Comment on the morphology of the erythrocytes.
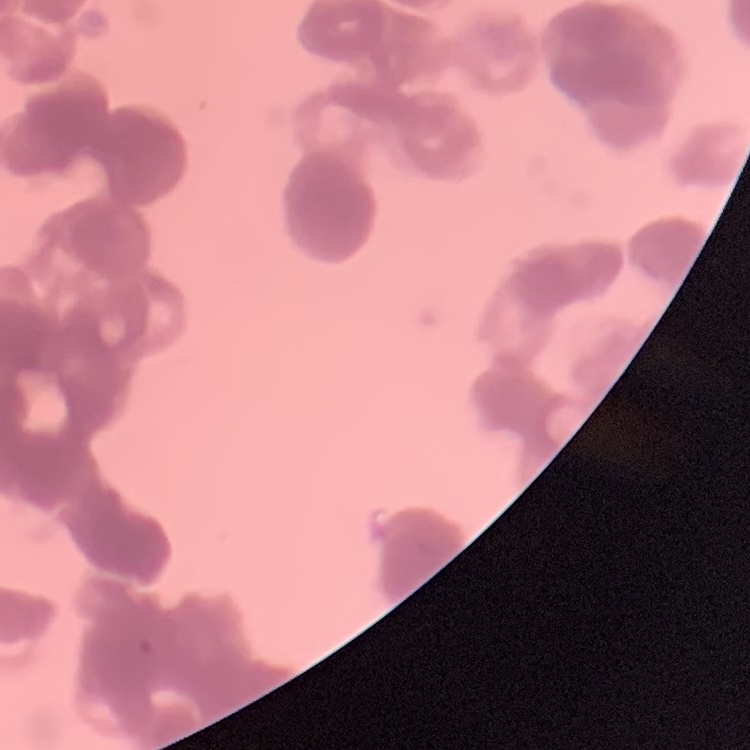

They show rouleaux formation.

One tile cut from a larger photomicrograph. Stained with either Field's or Giemsa. Thin peripheral smear.